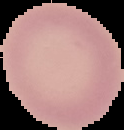
Summary:
  - Image size: 124×130 pixels
  - Preparation: thin blood smear
  - Result: no malaria parasites detected
  - Image type: cell region segmented out of the field of view; surrounding area masked to black